Name the cell type shown.
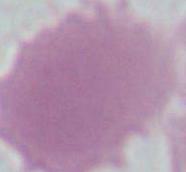
This is an erythrocyte.

Summary:
  - Magnification: 1000x
  - Modality: micrograph